Evaluate for malaria.
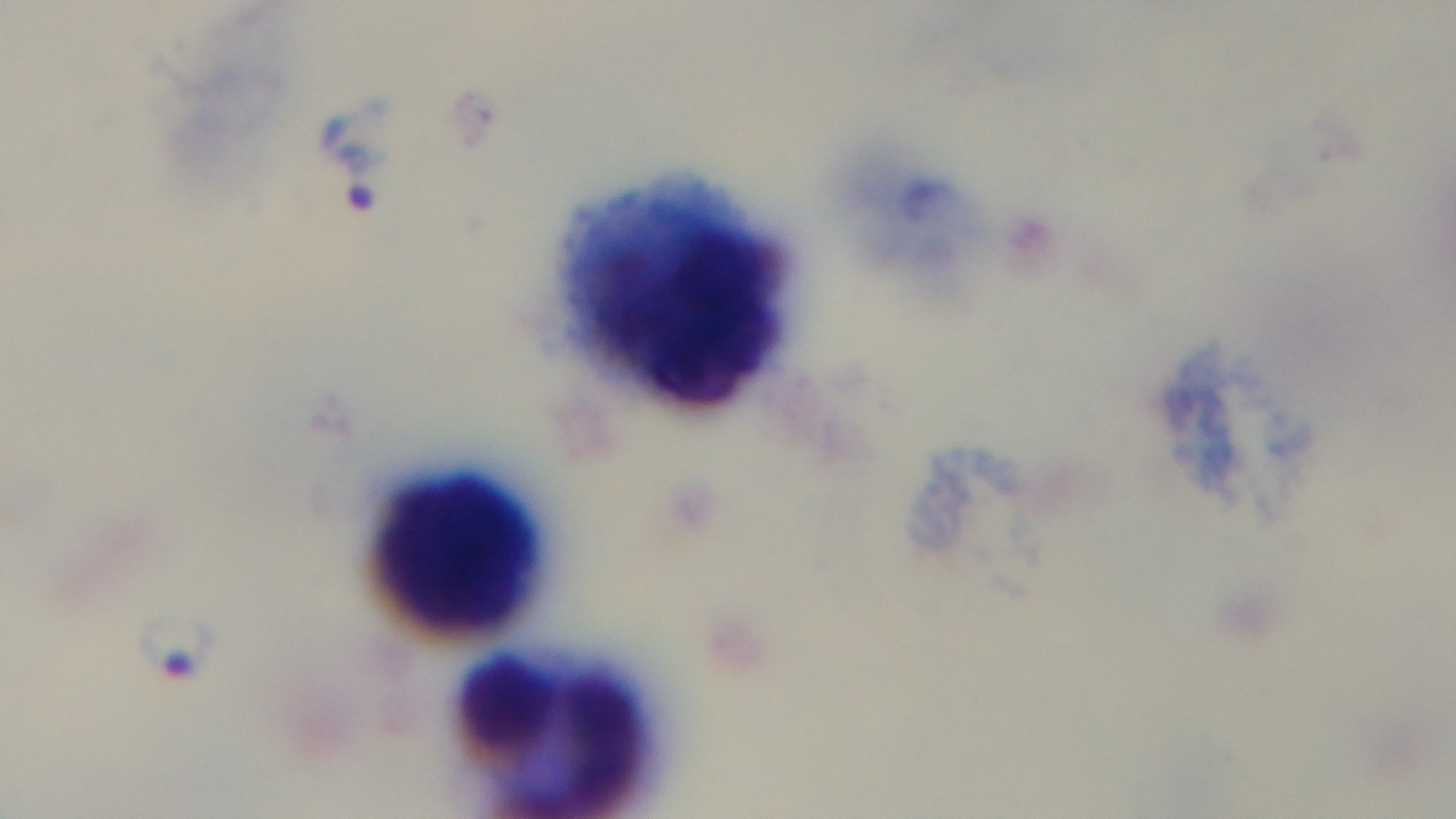
It is infected.

Summary:
  - Field of view: one from the slide
  - Modality: light microscopy
  - Preparation: thick blood film
  - Objective: 100x oil immersion
  - Stain: Giemsa
  - Capture: mounted 4K digital camera